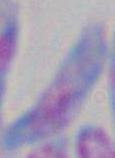

Summary:
  - Identification: Toxoplasma gondii
  - Magnification: 1000x
  - Modality: photomicrograph